Report the malaria status of this cell.
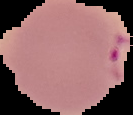

It is parasitized.

Summary:
  - Image size: 133×115 pixels
  - Preparation: thin blood smear
  - Image type: segmented cell region on a black background